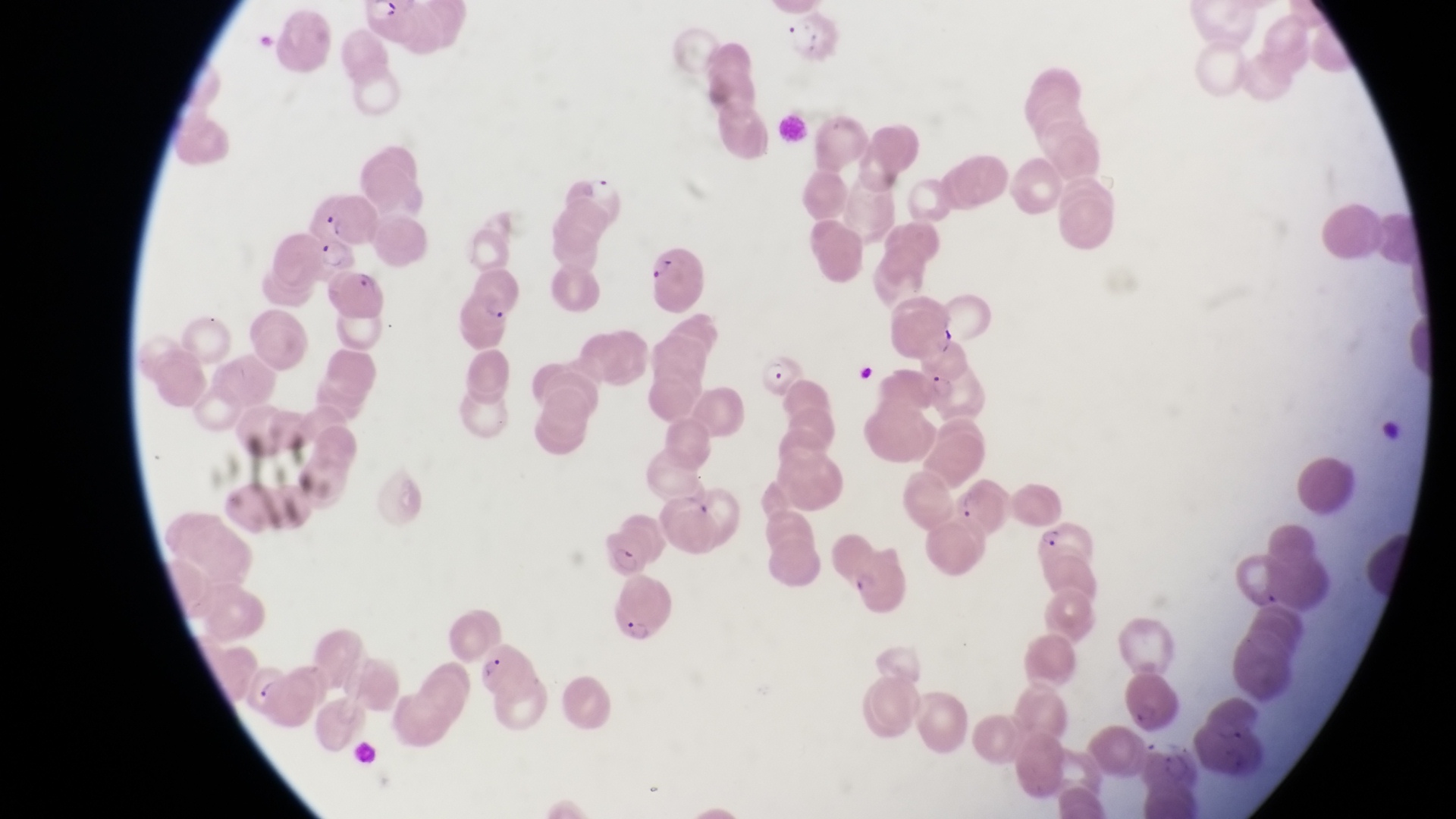

country = Uganda
preparation = thin blood smear
capture = smartphone photograph through the eyepiece of an Olympus CX-23 microscope
image size = 1456×819 pixels
magnification = 1000x
field of view = single
leukocyte locations = approximate bounding boxes as [left, top, right, bottom] in pixels: [1376, 409, 1408, 449]
parasitised red blood cell locations = approximate bounding boxes as [left, top, right, bottom] in pixels: [318, 235, 360, 277], [644, 245, 704, 311], [327, 267, 393, 325], [457, 284, 513, 327], [761, 354, 810, 400], [912, 359, 986, 418], [1033, 518, 1099, 564], [607, 525, 649, 580], [845, 555, 919, 619], [610, 579, 683, 653], [478, 645, 539, 701]